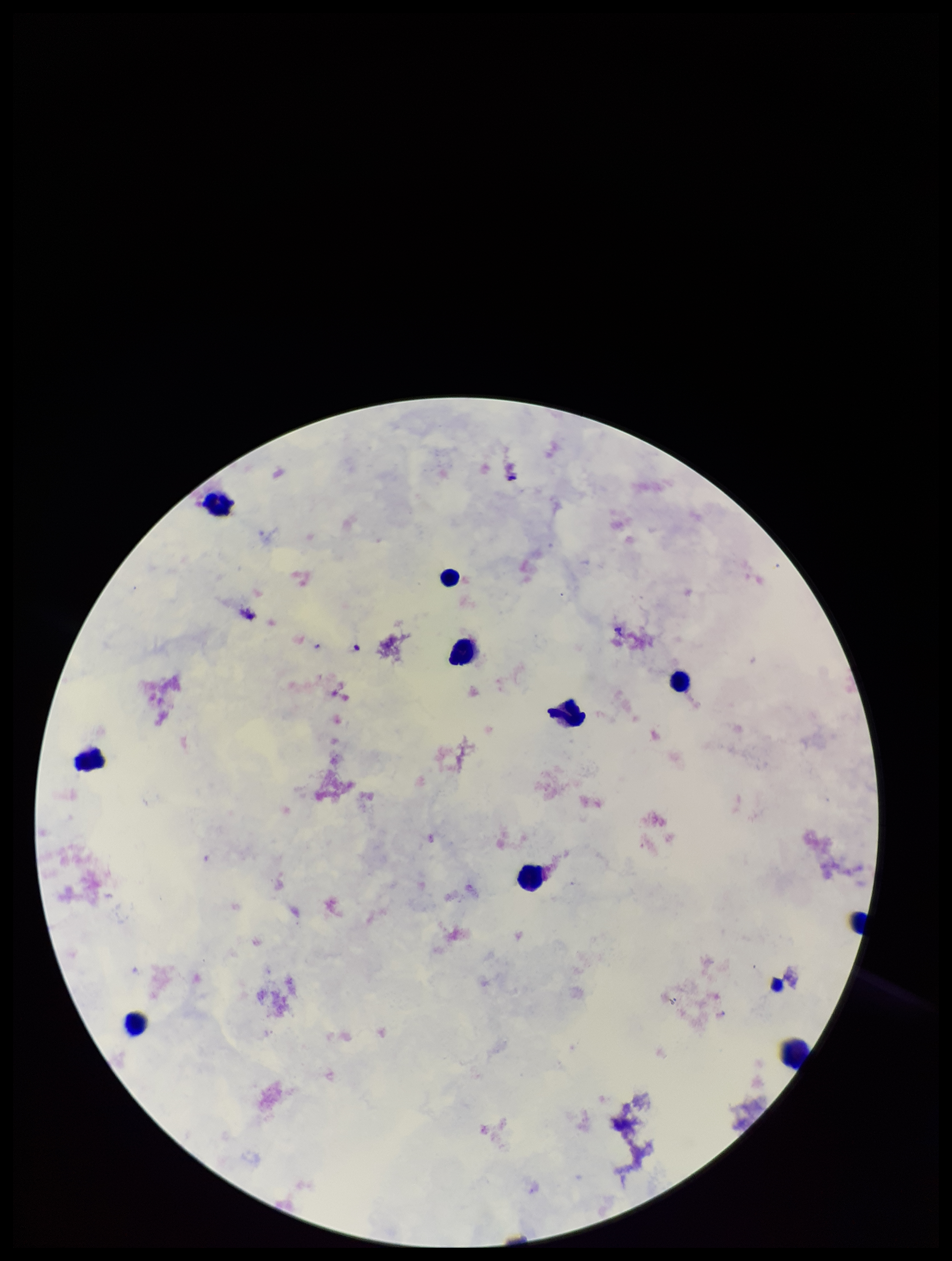
preparation = thick blood smear
parasite count = 0
stain = Giemsa
leukocyte count = 10
field of view = one from this slide
image size = 952×1261 pixels
Plasmodium parasites = none seen
capture = smartphone photograph through the microscope eyepiece
patient malaria status = negative